Assess this cell for malaria.
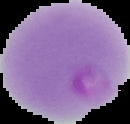
It is parasitized.

Image is 130×124 pixels. Cell region segmented out of the field of view; the surrounding area is masked to black. From a thin blood film.